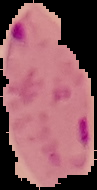 Segmented cell region on a black background. Malaria status: parasitized. From a thin blood smear. Image is 97×190 pixels.